Assess the morphology of the red blood cells.
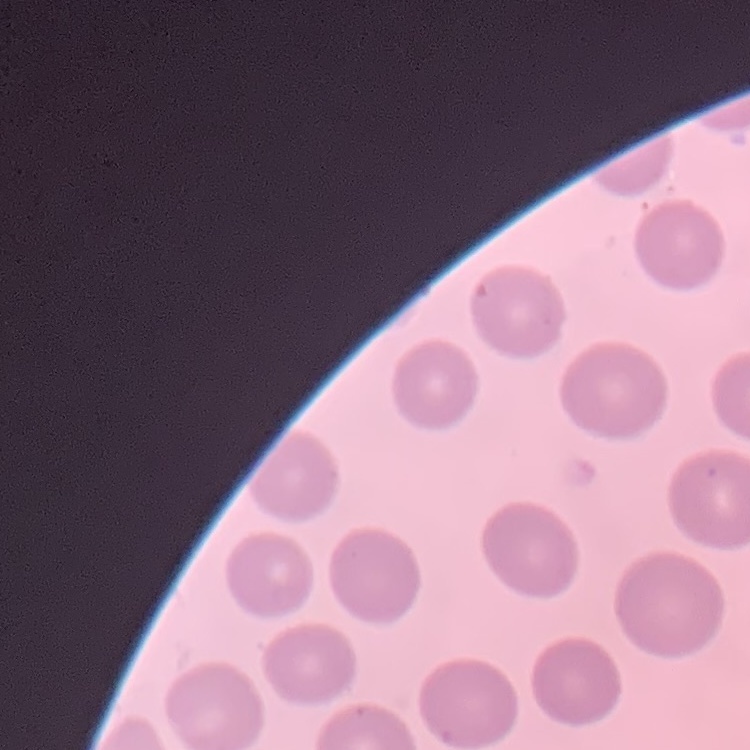
No rouleaux formation.

Summary:
  - Preparation: thin peripheral smear
  - Stain: Field's or Giemsa
  - Image type: square crop of a larger photomicrograph